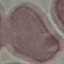 Malaria status: uninfected. Giemsa-stained preparation. Acquired by smartphone through the microscope eyepiece. Automatically extracted cell patch, resized to 64 × 64 pixels. Thin smear of blood.